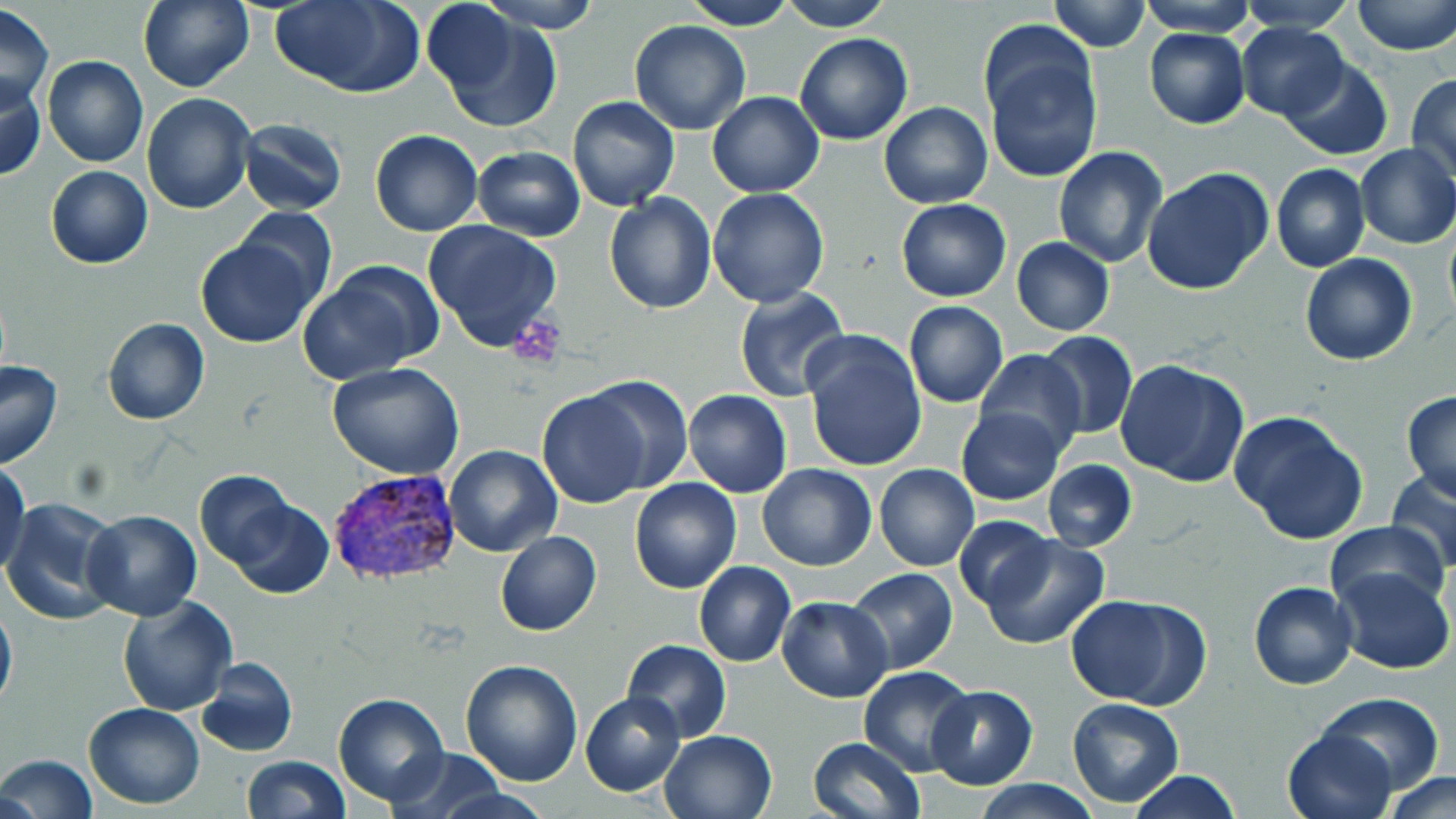 Approximate bounding boxes as (x1, y1, x2, y2) in pixels. Platelet locations: (510, 317, 564, 364). Plasmodium vivax-infected red blood cell locations: (325, 468, 462, 591). Uninfected red blood cell locations: (139, 0, 254, 92), (273, 0, 422, 97), (680, 0, 797, 31), (780, 0, 893, 30), (1047, 0, 1151, 52), (1139, 0, 1255, 36), (1351, 0, 1456, 56), (480, 1, 603, 33), (1234, 1, 1361, 32), (423, 3, 517, 97), (0, 4, 53, 112), (430, 9, 562, 133), (628, 21, 751, 136), (1236, 22, 1350, 122), (1143, 28, 1250, 129), (794, 31, 914, 144), (980, 37, 1103, 186), (42, 55, 148, 168), (1281, 58, 1392, 161), (1406, 74, 1456, 185), (0, 76, 45, 182), (707, 92, 825, 197), (142, 94, 255, 213), (566, 95, 680, 212), (877, 102, 992, 209), (239, 118, 348, 216), (370, 129, 482, 237), (1355, 143, 1456, 249), (1053, 145, 1168, 268), (471, 146, 585, 240), (1271, 163, 1370, 273), (45, 165, 153, 269), (1141, 167, 1275, 298), (707, 188, 829, 308), (603, 193, 716, 314), (897, 199, 1010, 301), (234, 208, 337, 307), (423, 220, 562, 350), (1444, 224, 1456, 329), (195, 236, 319, 348), (1012, 238, 1114, 336), (1300, 252, 1417, 365), (300, 265, 435, 381), (733, 287, 851, 402), (904, 301, 1007, 406), (102, 318, 210, 424), (802, 330, 928, 472), (1040, 330, 1137, 440), (975, 350, 1086, 458), (1116, 357, 1250, 488), (0, 360, 64, 468), (327, 364, 465, 480), (582, 375, 692, 493), (682, 388, 792, 498), (537, 390, 652, 509), (1401, 391, 1456, 503), (957, 406, 1065, 504), (1228, 410, 1370, 545), (443, 444, 563, 558), (0, 457, 29, 574), (1042, 460, 1137, 552), (756, 464, 877, 571), (874, 465, 979, 571), (1387, 469, 1456, 573), (194, 471, 300, 570), (629, 476, 742, 594), (228, 496, 334, 599), (3, 497, 122, 626), (80, 511, 201, 622), (953, 515, 1058, 613), (1324, 520, 1452, 617), (495, 531, 603, 636), (980, 531, 1111, 650), (694, 562, 796, 667), (844, 567, 959, 674), (1332, 567, 1454, 674), (1248, 580, 1359, 690), (1068, 593, 1212, 710), (116, 594, 237, 716), (776, 595, 893, 703), (0, 598, 17, 715), (621, 639, 731, 743), (196, 657, 298, 757), (460, 660, 584, 787), (859, 666, 975, 774), (927, 685, 1039, 787), (580, 692, 685, 795), (1316, 692, 1443, 792), (334, 693, 450, 807), (1065, 697, 1184, 807), (83, 702, 204, 810), (1283, 727, 1396, 819), (660, 729, 777, 819), (807, 736, 923, 819), (390, 747, 506, 818), (1, 754, 97, 819), (242, 755, 348, 818), (1126, 770, 1243, 819), (1379, 771, 1456, 819), (972, 779, 1103, 818). Slide-level diagnosis: Plasmodium vivax. Image is 1456×819 pixels. Light microscopy. Thin blood film. Single field of view. 1000x magnification. May-Grünwald-Giemsa-stained preparation.